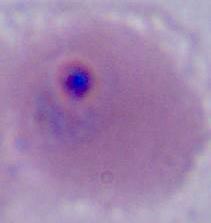

modality = micrograph
magnification = 400x or 1000x
identification = Plasmodium